Comment on the morphology of the red blood cells.
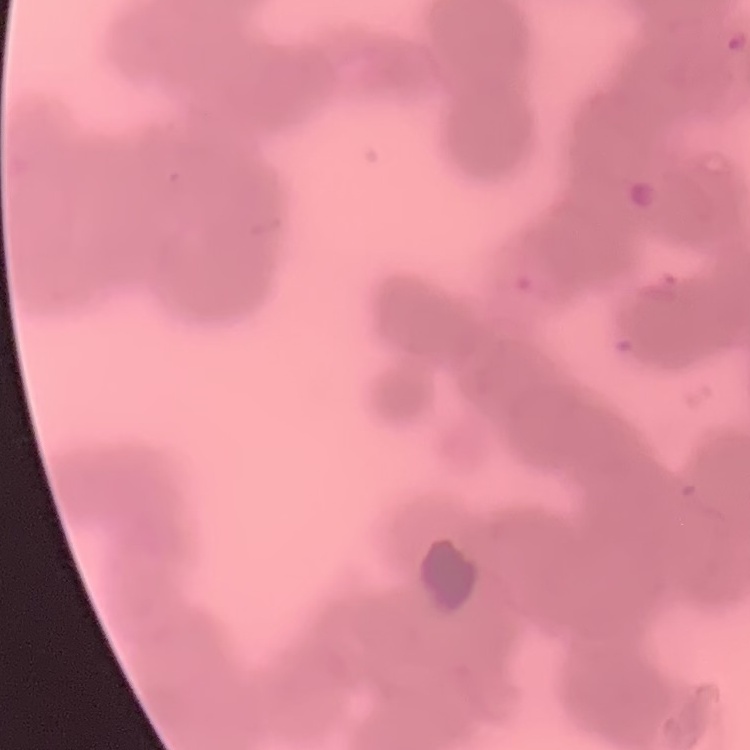
Rouleaux formation.

Summary:
  - Preparation: thin blood smear
  - Image type: square crop of a larger photomicrograph
  - Stain: Field's or Giemsa